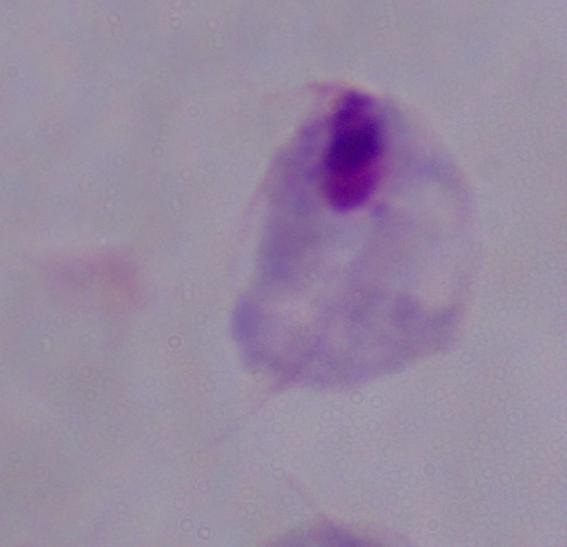

Summary:
  - Modality: micrograph
  - Magnification: 1000x
  - Identification: trichomonad